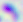
{
  "modality": "photomicrograph",
  "identification": "Toxoplasma gondii",
  "magnification": "400x"
}